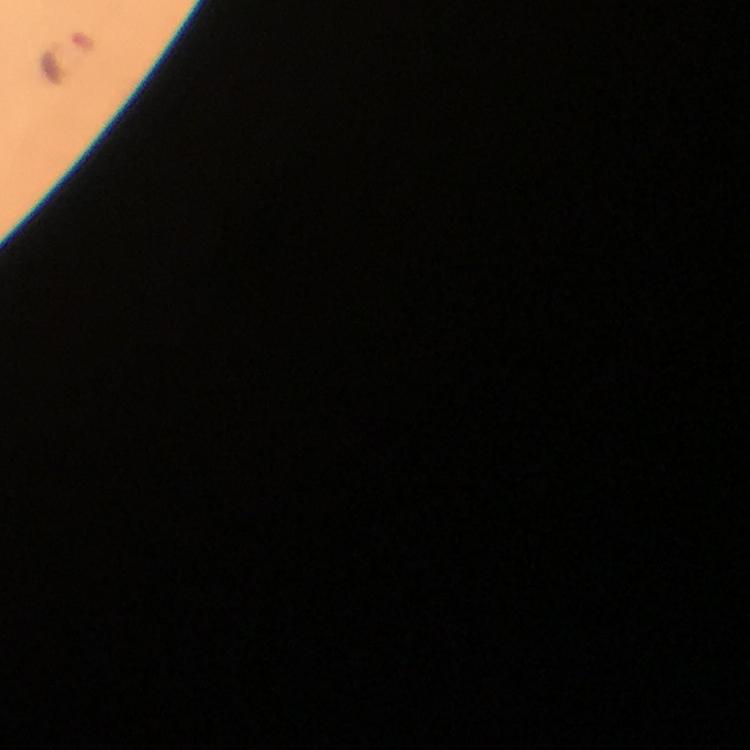

Approximate object centers, in pixels from the top-left corner.
Summary:
  - Malaria parasite locations: (x=68, y=52)
  - Image size: 750×750 pixels
  - Capture: smartphone camera through the microscope
  - Preparation: thick blood smear
  - Cropped from: a single field of view
  - Context: from a diagnostic examination for malaria
  - Magnification: 100x
  - Stain: Giemsa
  - Immersion oil: used